Describe the morphology of the red blood cells.
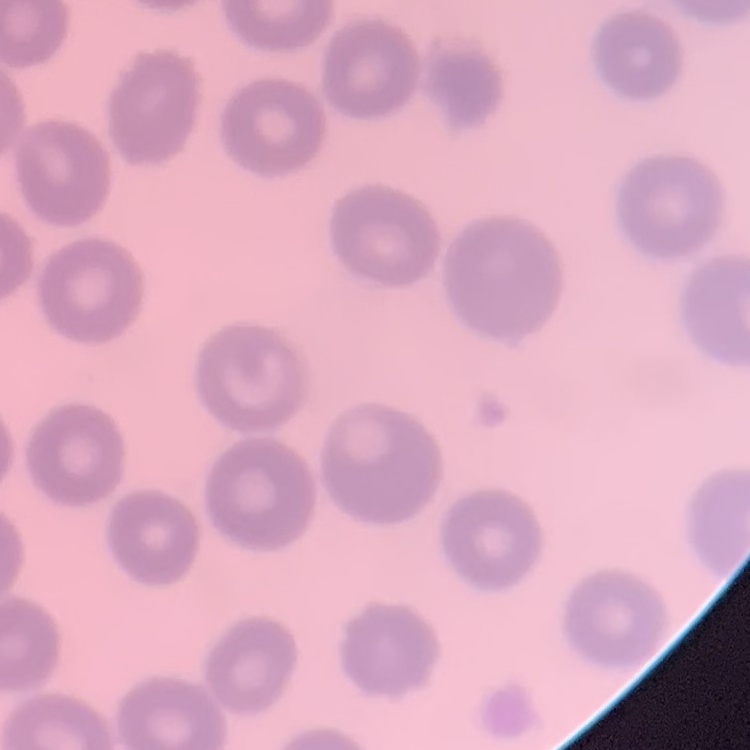

No rouleaux formation.

Summary:
  - Stain: Field's or Giemsa
  - Preparation: thin peripheral smear
  - Image type: square crop of a larger photomicrograph